Name the blood parasite species.
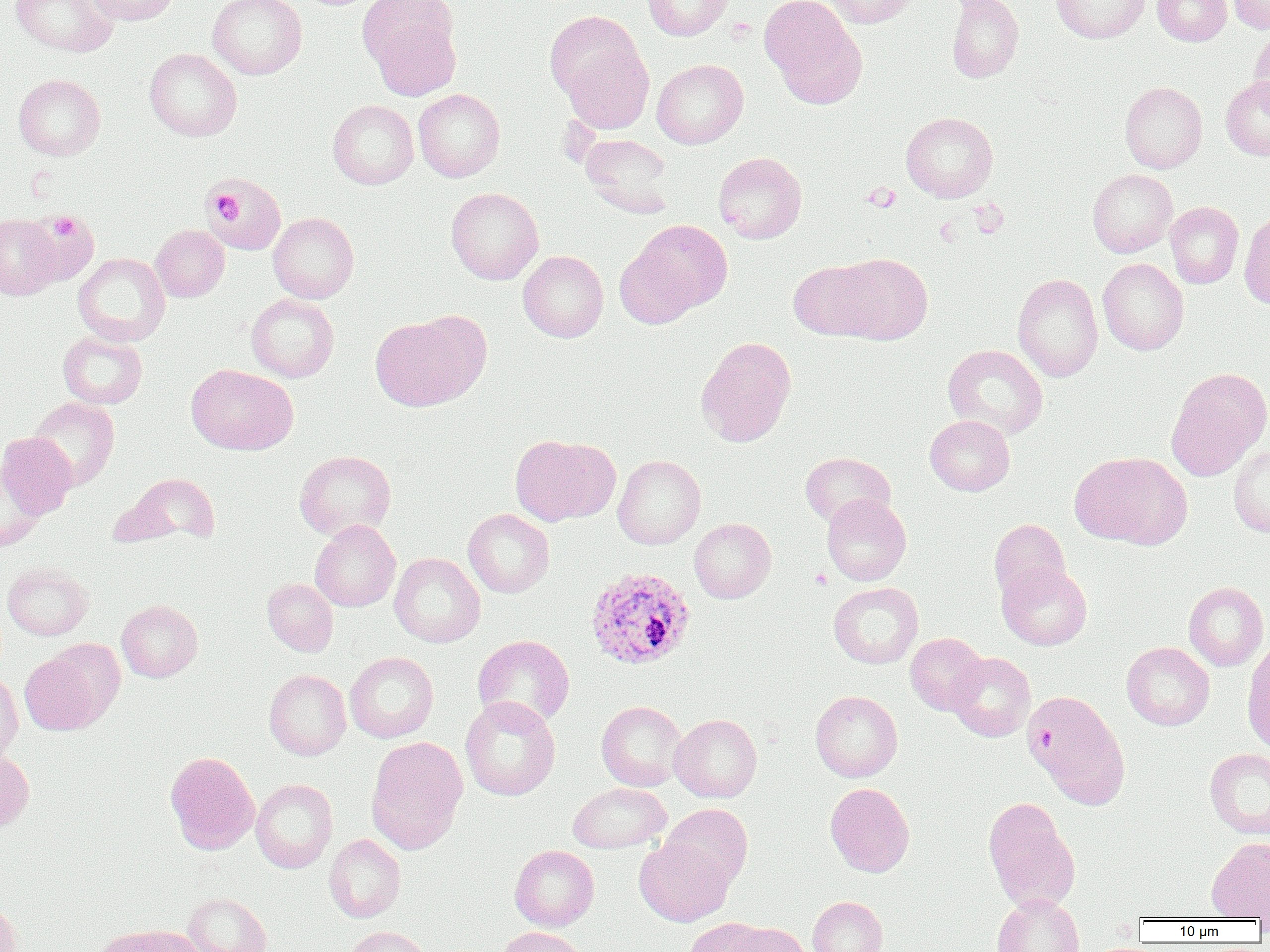

Plasmodium ovale.

Approximate bounding boxes as named x1/y1/x2/y2 corners in pixels. Uninfected red blood cell locations: (x1=9, y1=0, x2=119, y2=57), (x1=87, y1=0, x2=180, y2=26), (x1=208, y1=0, x2=307, y2=79), (x1=641, y1=0, x2=733, y2=41), (x1=760, y1=0, x2=866, y2=108), (x1=823, y1=0, x2=920, y2=27), (x1=946, y1=0, x2=1024, y2=82), (x1=1051, y1=0, x2=1150, y2=43), (x1=1152, y1=0, x2=1232, y2=46), (x1=1229, y1=0, x2=1270, y2=34), (x1=366, y1=8, x2=461, y2=102), (x1=1249, y1=25, x2=1270, y2=113), (x1=556, y1=27, x2=654, y2=133), (x1=144, y1=48, x2=241, y2=141), (x1=651, y1=59, x2=748, y2=149), (x1=13, y1=74, x2=105, y2=160), (x1=1220, y1=76, x2=1270, y2=160), (x1=1120, y1=81, x2=1207, y2=173), (x1=413, y1=89, x2=505, y2=182), (x1=328, y1=100, x2=419, y2=189), (x1=901, y1=112, x2=998, y2=202), (x1=580, y1=134, x2=675, y2=217), (x1=713, y1=152, x2=807, y2=244), (x1=1087, y1=169, x2=1177, y2=257), (x1=204, y1=170, x2=288, y2=255), (x1=446, y1=187, x2=543, y2=284), (x1=1165, y1=201, x2=1244, y2=288), (x1=25, y1=209, x2=99, y2=288), (x1=1239, y1=211, x2=1270, y2=310), (x1=268, y1=212, x2=359, y2=303), (x1=0, y1=214, x2=63, y2=299), (x1=622, y1=219, x2=733, y2=322), (x1=150, y1=225, x2=229, y2=302), (x1=518, y1=250, x2=608, y2=342), (x1=73, y1=253, x2=170, y2=346), (x1=831, y1=253, x2=933, y2=344), (x1=1098, y1=258, x2=1188, y2=355), (x1=788, y1=259, x2=885, y2=341), (x1=1012, y1=273, x2=1103, y2=381), (x1=246, y1=294, x2=339, y2=382), (x1=371, y1=312, x2=486, y2=411), (x1=58, y1=332, x2=147, y2=409), (x1=696, y1=336, x2=797, y2=447), (x1=943, y1=344, x2=1048, y2=439), (x1=186, y1=364, x2=297, y2=455), (x1=1165, y1=367, x2=1269, y2=481), (x1=29, y1=397, x2=119, y2=490), (x1=925, y1=415, x2=1015, y2=495), (x1=0, y1=432, x2=77, y2=518), (x1=509, y1=434, x2=619, y2=526), (x1=1228, y1=444, x2=1270, y2=538), (x1=294, y1=450, x2=396, y2=539), (x1=800, y1=452, x2=895, y2=528), (x1=1069, y1=452, x2=1189, y2=548), (x1=612, y1=454, x2=706, y2=549), (x1=0, y1=463, x2=45, y2=552), (x1=114, y1=471, x2=222, y2=548), (x1=822, y1=495, x2=911, y2=585), (x1=463, y1=509, x2=554, y2=597), (x1=689, y1=518, x2=776, y2=603), (x1=310, y1=519, x2=400, y2=612), (x1=989, y1=519, x2=1070, y2=601), (x1=389, y1=553, x2=485, y2=647), (x1=2, y1=562, x2=93, y2=641), (x1=997, y1=563, x2=1092, y2=650), (x1=262, y1=578, x2=338, y2=656), (x1=828, y1=582, x2=923, y2=669), (x1=1184, y1=582, x2=1269, y2=671), (x1=117, y1=600, x2=202, y2=682), (x1=905, y1=633, x2=987, y2=715), (x1=473, y1=635, x2=575, y2=728), (x1=1242, y1=639, x2=1270, y2=754), (x1=1121, y1=642, x2=1215, y2=730), (x1=20, y1=650, x2=111, y2=735), (x1=345, y1=652, x2=438, y2=743), (x1=948, y1=652, x2=1035, y2=742), (x1=264, y1=669, x2=351, y2=760), (x1=0, y1=672, x2=23, y2=762), (x1=1024, y1=689, x2=1131, y2=810), (x1=810, y1=690, x2=902, y2=782), (x1=460, y1=696, x2=560, y2=801), (x1=596, y1=701, x2=686, y2=791), (x1=670, y1=713, x2=761, y2=802), (x1=366, y1=736, x2=468, y2=855), (x1=1205, y1=747, x2=1270, y2=839), (x1=0, y1=749, x2=34, y2=834), (x1=165, y1=752, x2=259, y2=854), (x1=251, y1=778, x2=338, y2=873), (x1=567, y1=782, x2=671, y2=853), (x1=825, y1=783, x2=914, y2=877), (x1=983, y1=797, x2=1080, y2=913), (x1=661, y1=804, x2=752, y2=890), (x1=324, y1=834, x2=406, y2=922), (x1=1206, y1=837, x2=1270, y2=920), (x1=634, y1=838, x2=733, y2=927), (x1=510, y1=845, x2=599, y2=931), (x1=183, y1=892, x2=271, y2=952), (x1=992, y1=893, x2=1084, y2=952), (x1=807, y1=896, x2=887, y2=952), (x1=0, y1=899, x2=22, y2=952), (x1=683, y1=917, x2=773, y2=952), (x1=730, y1=923, x2=810, y2=952), (x1=101, y1=925, x2=203, y2=952), (x1=344, y1=926, x2=433, y2=952), (x1=494, y1=926, x2=588, y2=952). Platelet locations: (x1=862, y1=183, x2=899, y2=211), (x1=206, y1=188, x2=242, y2=222), (x1=969, y1=200, x2=1008, y2=238), (x1=49, y1=213, x2=80, y2=241), (x1=935, y1=218, x2=960, y2=245), (x1=811, y1=569, x2=831, y2=589). Plasmodium ovale-infected red blood cell locations: (x1=585, y1=567, x2=696, y2=670). One field of a larger specimen. Thin blood film. Optical microscopy. Image is 1270×952 pixels. Captured at 1000x magnification.